Locate and identify every blood parasite.
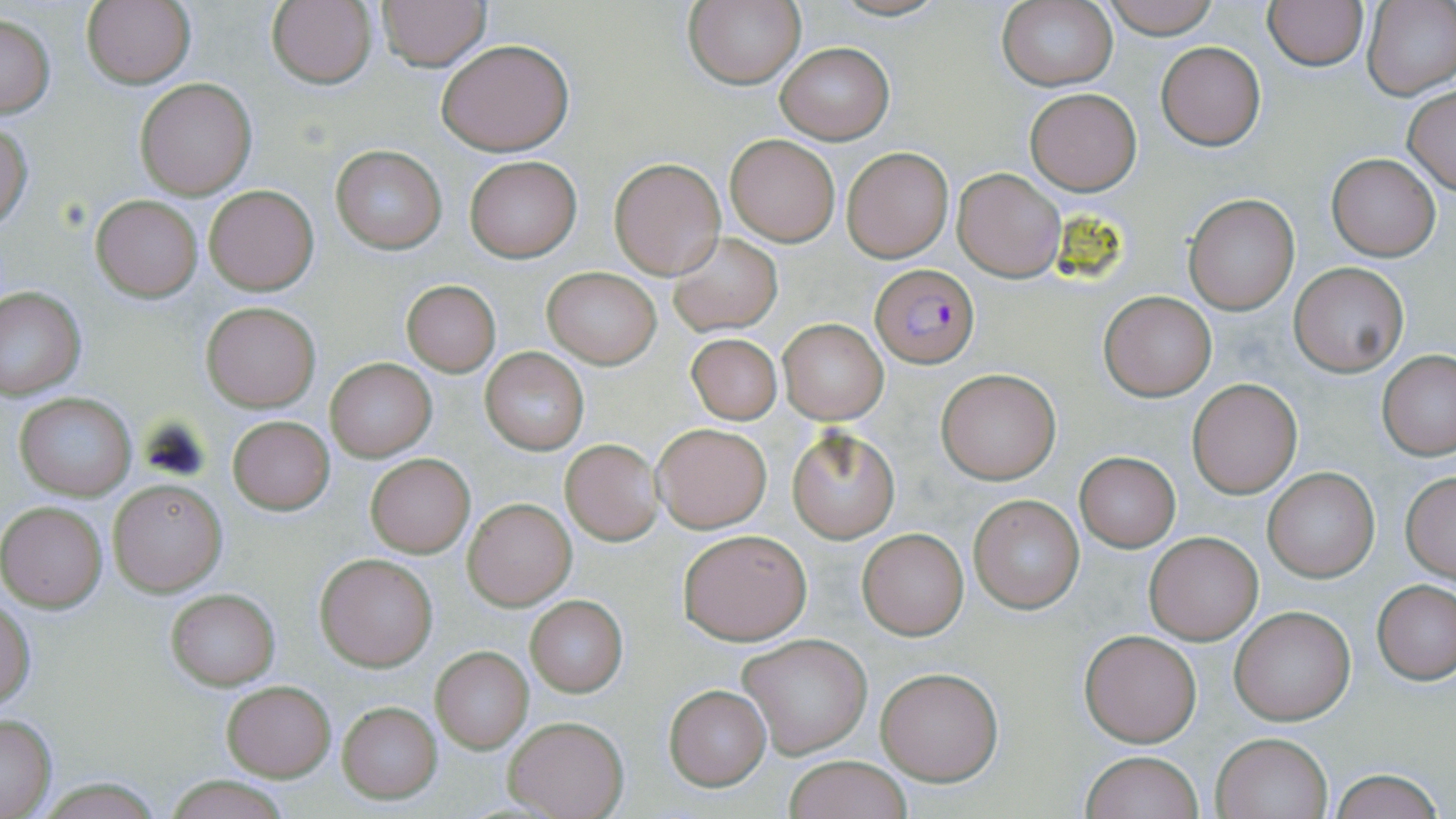
Approximate bounding boxes as [x1, y1, x2, y2] in pixels.
Plasmodium falciparum-infected red blood cells: [870, 263, 979, 368].
No Plasmodium ovale, Plasmodium malariae, Plasmodium vivax, Babesia divergens, or Trypanosoma brucei observed.

Summary:
  - Uninfected red blood cell locations: [82, 0, 196, 89], [267, 0, 376, 89], [373, 0, 492, 70], [1100, 0, 1221, 37], [1263, 0, 1370, 70], [995, 1, 1117, 91], [1362, 1, 1455, 101], [682, 2, 806, 88], [1, 14, 55, 119], [435, 38, 575, 156], [776, 42, 894, 144], [1155, 42, 1266, 150], [135, 77, 257, 199], [1403, 86, 1455, 195], [1024, 89, 1141, 195], [0, 123, 34, 232], [724, 134, 839, 245], [331, 145, 445, 253], [842, 147, 953, 262], [1327, 154, 1440, 260], [464, 156, 581, 262], [610, 158, 725, 278], [954, 168, 1065, 281], [203, 183, 320, 295], [92, 195, 202, 301], [1184, 195, 1298, 315], [668, 233, 782, 335], [1290, 263, 1407, 376], [542, 267, 661, 368], [401, 280, 500, 376], [0, 285, 86, 397], [1100, 292, 1216, 400], [202, 302, 320, 411], [778, 319, 888, 423], [686, 332, 782, 425], [481, 349, 588, 453], [1378, 351, 1456, 460], [325, 358, 437, 460], [938, 370, 1058, 481], [1188, 378, 1301, 498], [15, 394, 137, 498], [226, 416, 335, 515], [652, 423, 772, 533], [788, 428, 899, 542], [560, 439, 663, 545], [365, 453, 474, 557], [1074, 454, 1180, 553], [1262, 466, 1379, 583], [1401, 473, 1456, 580], [109, 479, 226, 596], [968, 494, 1084, 612], [463, 498, 575, 609], [0, 501, 108, 611], [677, 528, 812, 645], [857, 529, 968, 640], [1145, 532, 1261, 643], [315, 553, 437, 670], [1373, 580, 1454, 685], [164, 587, 281, 690], [525, 596, 627, 696], [0, 599, 36, 710], [1229, 606, 1356, 724], [1078, 628, 1201, 746], [738, 633, 872, 757], [430, 647, 533, 751], [876, 665, 1003, 785], [220, 680, 336, 781], [664, 685, 771, 789], [336, 701, 441, 803], [0, 712, 57, 818], [505, 716, 628, 819], [1212, 732, 1332, 817], [1081, 750, 1202, 819], [781, 755, 915, 818], [1330, 768, 1445, 819], [165, 775, 292, 818]
  - Slide-level diagnosis: Plasmodium falciparum
  - Preparation: thin blood film
  - Modality: light microscopy
  - Stain: May-Grünwald-Giemsa
  - Magnification: 1000x
  - Field of view: one of a larger specimen
  - Image size: 1456×819 pixels